Assess this cell for malaria.
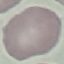

Uninfected.

Summary:
  - Image type: cell patch, automatically extracted from a larger field of view and resized to 64 × 64 pixels
  - Stain: Giemsa
  - Preparation: thin blood film
  - Capture: smartphone camera at the microscope eyepiece